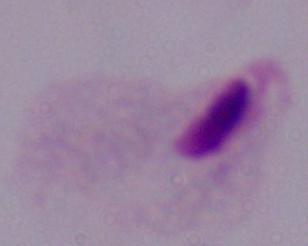
identification = trichomonad
magnification = 1000x
modality = micrograph